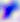

{
  "identification": "Toxoplasma gondii",
  "modality": "micrograph",
  "magnification": "400x"
}